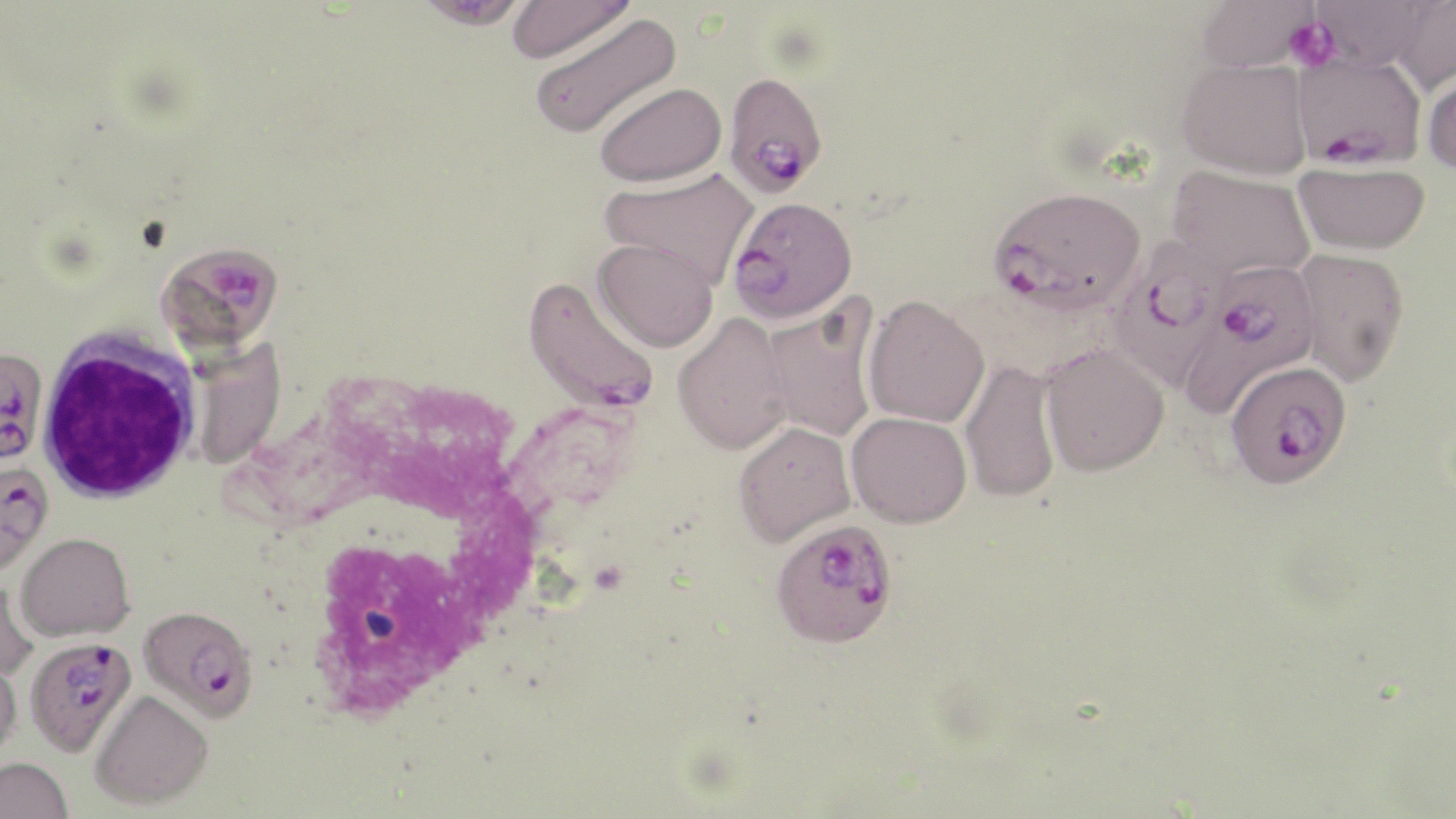 Approximate bounding boxes as (x1,y1)-(x2,y2) corner pairs in pixels. White blood cell locations: (35,326)-(203,505). Platelet locations: (1284,16)-(1340,71). Plasmodium falciparum-infected red blood cell locations: (1292,53)-(1427,170), (722,71)-(828,198), (988,185)-(1147,314), (727,195)-(858,324), (1106,235)-(1231,391), (158,240)-(285,355), (1183,259)-(1320,416), (523,276)-(661,414), (0,347)-(49,467), (1225,360)-(1353,488), (0,455)-(54,576), (769,518)-(899,648), (138,605)-(258,722), (25,636)-(138,757). Uninfected red blood cell locations: (505,0)-(636,64), (1195,0)-(1319,73), (1390,0)-(1456,97), (413,1)-(532,31), (1308,1)-(1433,72), (528,12)-(681,140), (1178,58)-(1311,180), (1422,66)-(1456,176), (594,81)-(726,187), (1293,161)-(1430,256), (1167,166)-(1316,281), (599,167)-(759,286), (593,237)-(719,352), (1292,247)-(1409,385), (862,295)-(989,428), (760,300)-(879,444), (672,313)-(793,456), (1040,343)-(1169,477), (959,360)-(1062,503), (846,411)-(972,528), (732,421)-(856,547), (16,532)-(134,641), (0,580)-(41,681), (0,657)-(22,765), (89,690)-(213,810), (0,757)-(73,819). Slide-level diagnosis: Plasmodium falciparum. Single field of view. Image is 1456×819 pixels. May-Grünwald-Giemsa stain. Captured at 1000x magnification. Thin blood film. Optical microscopy.